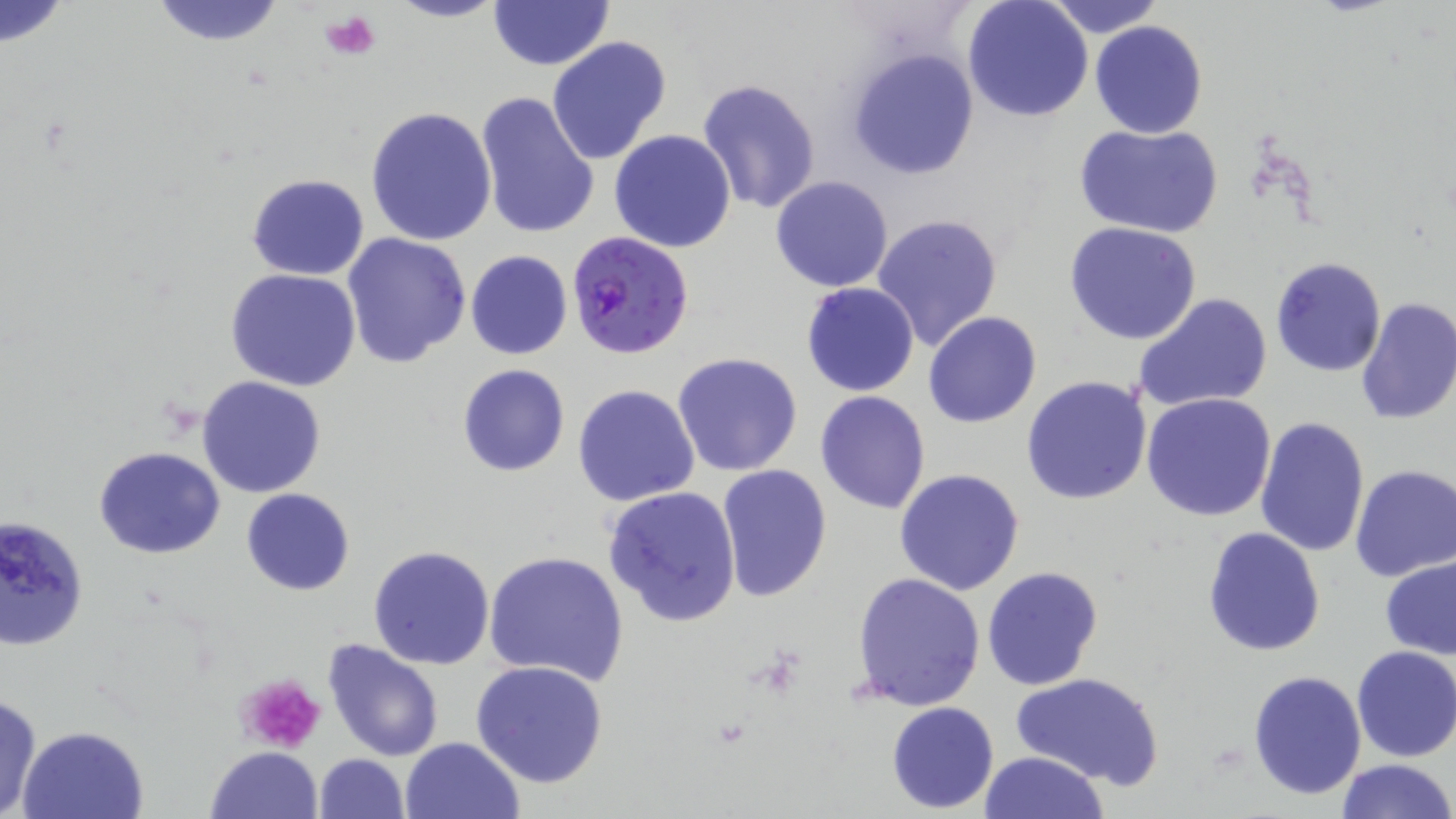
slide-level diagnosis = Plasmodium falciparum
field of view = one of a larger specimen
modality = optical microscopy
uninfected red blood cell locations = approximate bounding boxes as (x1,y1)-(x2,y2) corner pairs in pixels: (148,0)-(288,46), (387,0)-(506,24), (486,0)-(614,71), (962,0)-(1093,121), (1042,0)-(1165,37), (0,1)-(71,49), (1089,21)-(1207,139), (545,36)-(671,165), (848,50)-(978,180), (696,78)-(822,215), (474,91)-(599,238), (365,107)-(497,248), (1076,125)-(1221,240), (609,129)-(736,252), (246,174)-(369,280), (770,176)-(895,292), (872,212)-(1004,353), (1064,223)-(1204,346), (344,233)-(473,368), (465,250)-(573,361), (1271,255)-(1387,378), (225,269)-(362,392), (801,282)-(920,396), (1133,291)-(1273,414), (1354,298)-(1456,427), (922,312)-(1042,428), (672,352)-(803,477), (457,364)-(569,477), (1020,375)-(1152,505), (197,376)-(327,497), (572,384)-(700,506), (814,390)-(930,513), (1142,391)-(1277,521), (1255,415)-(1369,559), (95,446)-(226,559), (1350,464)-(1456,583), (716,465)-(832,601), (895,469)-(1025,594), (604,486)-(742,626), (241,488)-(354,595), (0,516)-(90,654), (1203,526)-(1326,658), (368,544)-(495,668), (484,549)-(629,684), (1379,552)-(1456,660), (981,566)-(1103,690), (851,571)-(985,711), (322,638)-(445,761), (1351,645)-(1456,763), (470,660)-(609,789), (1246,668)-(1367,801), (1011,672)-(1164,789), (0,693)-(44,818), (886,701)-(999,813), (17,724)-(150,818), (400,737)-(525,819), (206,746)-(324,819), (979,750)-(1110,819), (314,753)-(409,819), (1335,758)-(1454,819)
magnification = 1000x
platelet locations = approximate bounding boxes as (x1,y1)-(x2,y2) corner pairs in pixels: (320,11)-(380,60), (236,671)-(328,754)
Plasmodium falciparum-infected red blood cell locations = approximate bounding boxes as (x1,y1)-(x2,y2) corner pairs in pixels: (566,231)-(694,359)
stain = May-Grünwald-Giemsa
image size = 1456×819 pixels
preparation = thin blood smear